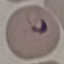

result = malaria parasites detected
capture = smartphone camera at the microscope eyepiece
preparation = thin smear
stain = Giemsa
image type = automatically extracted cell patch, resized to 64 × 64 pixels